Identify the parasite.
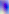

Toxoplasma gondii.

Micrograph. 400x magnification.